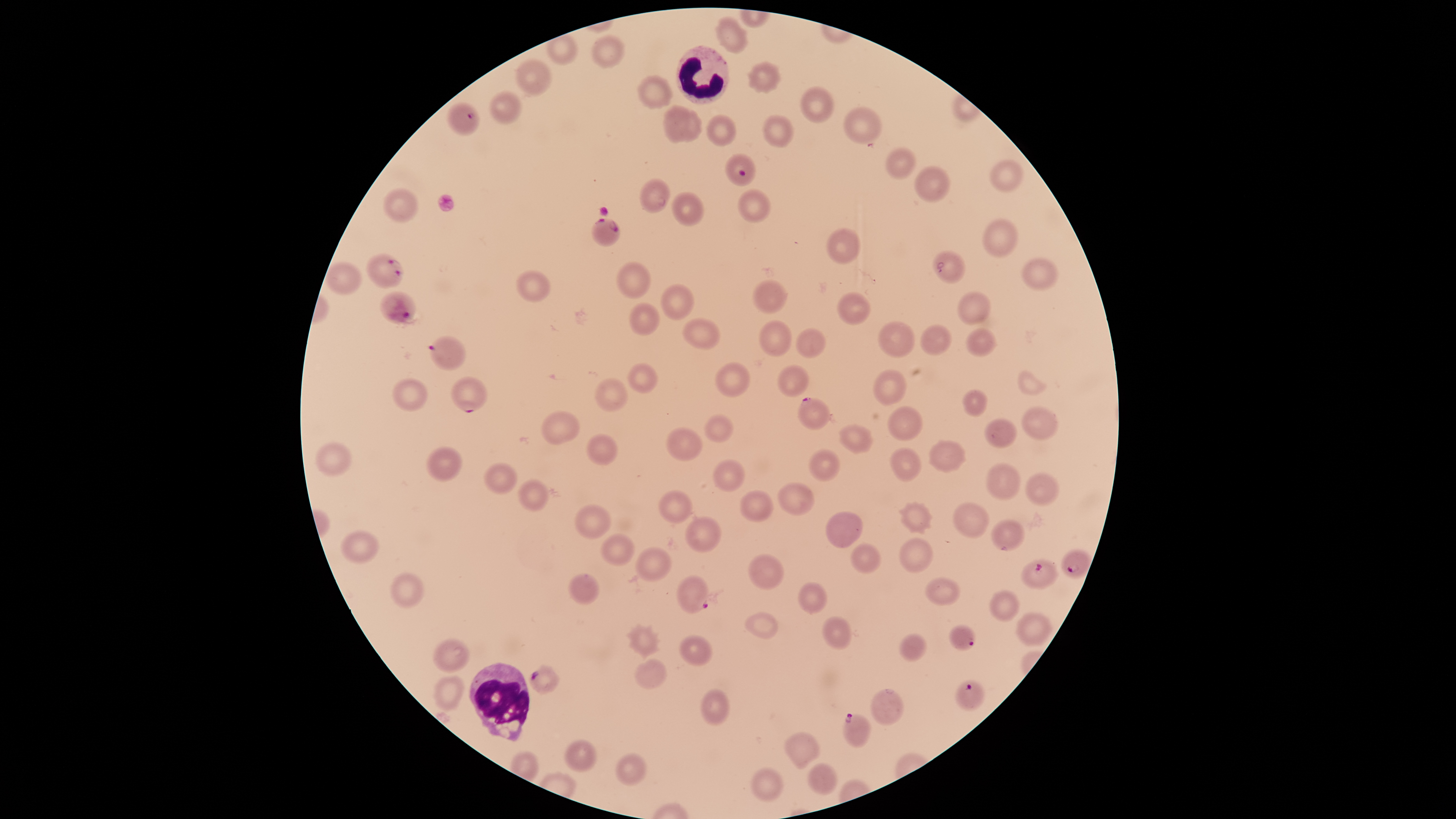

Approximate bounding boxes as {left, top, right, bottom} in pixels.
Summary:
  - Parasitized RBCs: {446, 103, 480, 136}, {725, 154, 756, 186}, {591, 218, 620, 247}, {366, 254, 403, 288}, {380, 291, 417, 325}, {428, 336, 465, 370}, {451, 376, 487, 413}, {798, 397, 832, 430}, {1061, 548, 1093, 579}, {1021, 559, 1059, 589}, {676, 575, 708, 614}, {949, 625, 975, 651}, {528, 664, 560, 695}, {956, 680, 984, 711}, {843, 713, 872, 747}
  - WBCs: {676, 46, 729, 105}, {469, 662, 530, 742}
  - Uninfected RBCs: {715, 18, 748, 53}, {592, 35, 625, 68}, {515, 59, 552, 97}, {747, 61, 781, 93}, {637, 75, 673, 109}, {799, 86, 833, 123}, {489, 91, 522, 124}, {663, 106, 690, 143}, {843, 106, 882, 144}, {674, 111, 702, 142}, {707, 115, 736, 146}, {763, 116, 794, 147}, {885, 148, 916, 179}, {989, 160, 1024, 191}, {914, 166, 951, 202}, {639, 178, 670, 213}, {383, 188, 417, 223}, {738, 189, 770, 223}, {671, 192, 704, 227}, {982, 218, 1018, 257}, {826, 228, 862, 264}, {932, 250, 966, 284}, {1021, 258, 1060, 290}, {327, 263, 362, 295}, {617, 263, 650, 299}, {516, 269, 550, 302}, {752, 280, 787, 314}, {661, 284, 693, 320}, {836, 292, 871, 325}, {957, 292, 991, 325}, {629, 303, 660, 336}, {682, 317, 720, 350}, {758, 320, 792, 357}, {877, 321, 915, 359}, {920, 325, 952, 355}, {796, 328, 826, 358}, {966, 328, 997, 357}, {715, 362, 749, 397}, {628, 363, 657, 393}, {777, 364, 809, 397}, {872, 370, 907, 406}, {1018, 371, 1045, 397}, {392, 378, 427, 412}, {595, 378, 627, 412}, {962, 389, 987, 417}, {887, 406, 923, 441}, {1021, 406, 1057, 439}, {540, 411, 579, 445}, {705, 414, 734, 443}, {984, 419, 1017, 448}, {838, 424, 874, 453}, {667, 428, 702, 461}, {586, 434, 617, 465}, {928, 440, 966, 472}, {314, 442, 352, 475}, {426, 446, 462, 481}, {890, 448, 922, 482}, {808, 449, 840, 482}, {712, 460, 745, 492}, {484, 462, 517, 494}, {986, 463, 1020, 500}, {1024, 474, 1060, 506}, {517, 479, 547, 512}, {777, 482, 814, 516}, {658, 490, 692, 524}, {740, 490, 773, 523}, {899, 502, 933, 534}, {953, 503, 989, 538}, {574, 504, 611, 539}, {826, 512, 862, 547}, {685, 516, 721, 552}, {991, 519, 1025, 552}, {341, 530, 380, 563}, {600, 533, 634, 566}, {899, 538, 933, 572}, {850, 543, 881, 573}, {635, 547, 672, 581}, {748, 554, 784, 590}, {390, 571, 424, 608}, {568, 573, 600, 605}, {924, 578, 960, 605}, {797, 581, 827, 614}, {989, 590, 1020, 621}, {744, 612, 779, 639}, {1016, 612, 1051, 646}, {822, 616, 851, 650}, {629, 625, 658, 656}, {899, 633, 927, 662}, {679, 636, 712, 665}, {432, 638, 470, 672}, {634, 659, 667, 689}, {435, 675, 463, 710}, {701, 689, 729, 726}, {871, 689, 904, 726}, {785, 732, 819, 768}, {564, 740, 596, 772}, {615, 752, 645, 786}, {808, 763, 837, 795}, {751, 767, 784, 802}
  - Visible region: circular
  - Field of view: single
  - Image size: 1456×819 pixels
  - Stain: Giemsa
  - Capture: smartphone photograph through the microscope eyepiece
  - Species: Plasmodium falciparum
  - Presence: malaria parasites seen
  - Preparation: thin smear of blood